Report the malaria status.
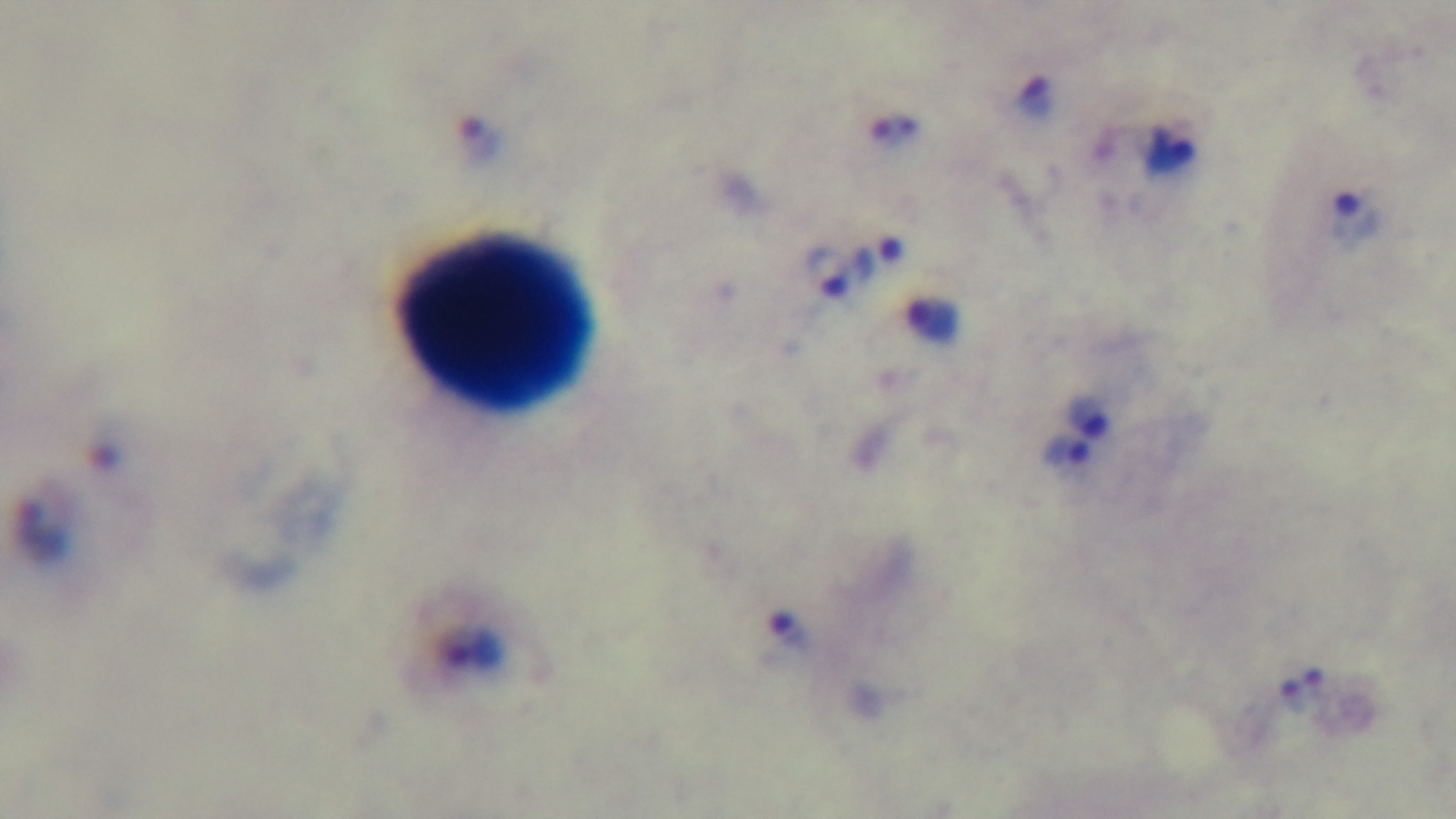
It is infected.

Summary:
  - Stain: Giemsa
  - Capture: mounted 4K digital camera
  - Field of view: single
  - Objective: 100x oil immersion
  - Modality: light microscopy
  - Preparation: thick blood film